State which cell type is depicted.
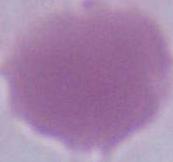

This is an erythrocyte.

{
  "modality": "micrograph",
  "magnification": "1000x"
}